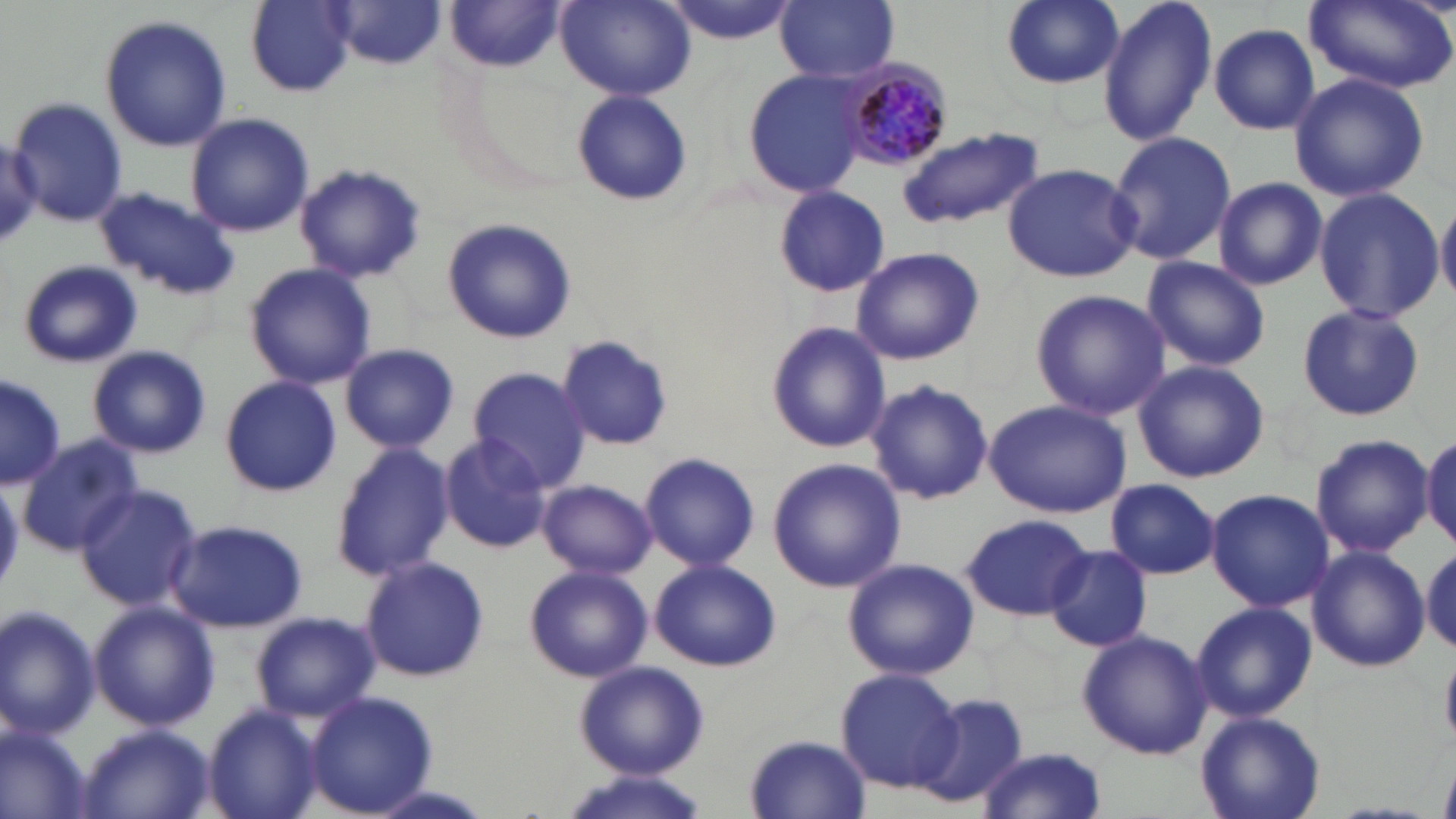

Plasmodium malariae-infected red blood cell locations = approximate bounding boxes as (x1, y1, x2, y2) in pixels: (844, 62, 956, 170)
slide-level diagnosis = Plasmodium malariae
preparation = thin blood smear
field of view = one of a larger specimen
uninfected red blood cell locations = approximate bounding boxes as (x1, y1, x2, y2) in pixels: (245, 0, 355, 95), (776, 0, 899, 83), (999, 0, 1124, 89), (1095, 0, 1218, 148), (557, 1, 693, 102), (660, 1, 803, 44), (1306, 1, 1453, 93), (330, 2, 448, 67), (445, 3, 563, 72), (100, 15, 230, 152), (1208, 24, 1319, 135), (743, 68, 870, 199), (1289, 72, 1429, 203), (571, 89, 692, 206), (8, 96, 127, 226), (186, 114, 314, 238), (900, 127, 1041, 229), (1106, 131, 1237, 266), (1002, 163, 1142, 282), (293, 164, 427, 283), (1212, 177, 1327, 290), (94, 186, 240, 300), (772, 186, 889, 295), (1311, 187, 1444, 323), (1436, 198, 1456, 305), (443, 216, 578, 344), (850, 246, 985, 366), (1140, 256, 1271, 372), (17, 259, 143, 368), (244, 263, 376, 391), (1029, 288, 1171, 422), (1296, 303, 1424, 421), (766, 319, 889, 453), (557, 334, 675, 452), (87, 344, 211, 459), (339, 344, 461, 453), (1133, 359, 1269, 483), (468, 367, 591, 492), (1, 373, 64, 489), (220, 375, 341, 497), (866, 380, 993, 505), (986, 399, 1132, 518), (19, 433, 142, 556), (439, 434, 553, 555), (1310, 434, 1433, 557), (1422, 434, 1456, 548), (330, 444, 454, 580), (638, 452, 760, 571), (767, 459, 906, 594), (1105, 478, 1222, 580), (537, 479, 656, 579), (73, 485, 202, 611), (1204, 488, 1333, 611), (960, 513, 1093, 622), (168, 519, 307, 633), (1044, 544, 1154, 653), (1307, 544, 1429, 672), (1422, 545, 1456, 655), (360, 555, 489, 683), (843, 557, 980, 680), (651, 559, 781, 671), (523, 564, 653, 682), (1191, 602, 1317, 722), (91, 603, 218, 730), (0, 605, 101, 740), (252, 612, 377, 722), (1076, 629, 1212, 760), (1440, 644, 1456, 741), (574, 661, 708, 779), (836, 668, 961, 790), (305, 690, 439, 817), (910, 692, 1028, 810), (203, 705, 324, 819), (1196, 711, 1326, 819), (0, 724, 90, 818), (78, 725, 213, 818), (744, 734, 870, 817), (977, 746, 1108, 819), (558, 769, 713, 819)
modality = light microscopy
magnification = 1000x
image size = 1456×819 pixels
stain = May-Grünwald-Giemsa